Evaluate for malaria.
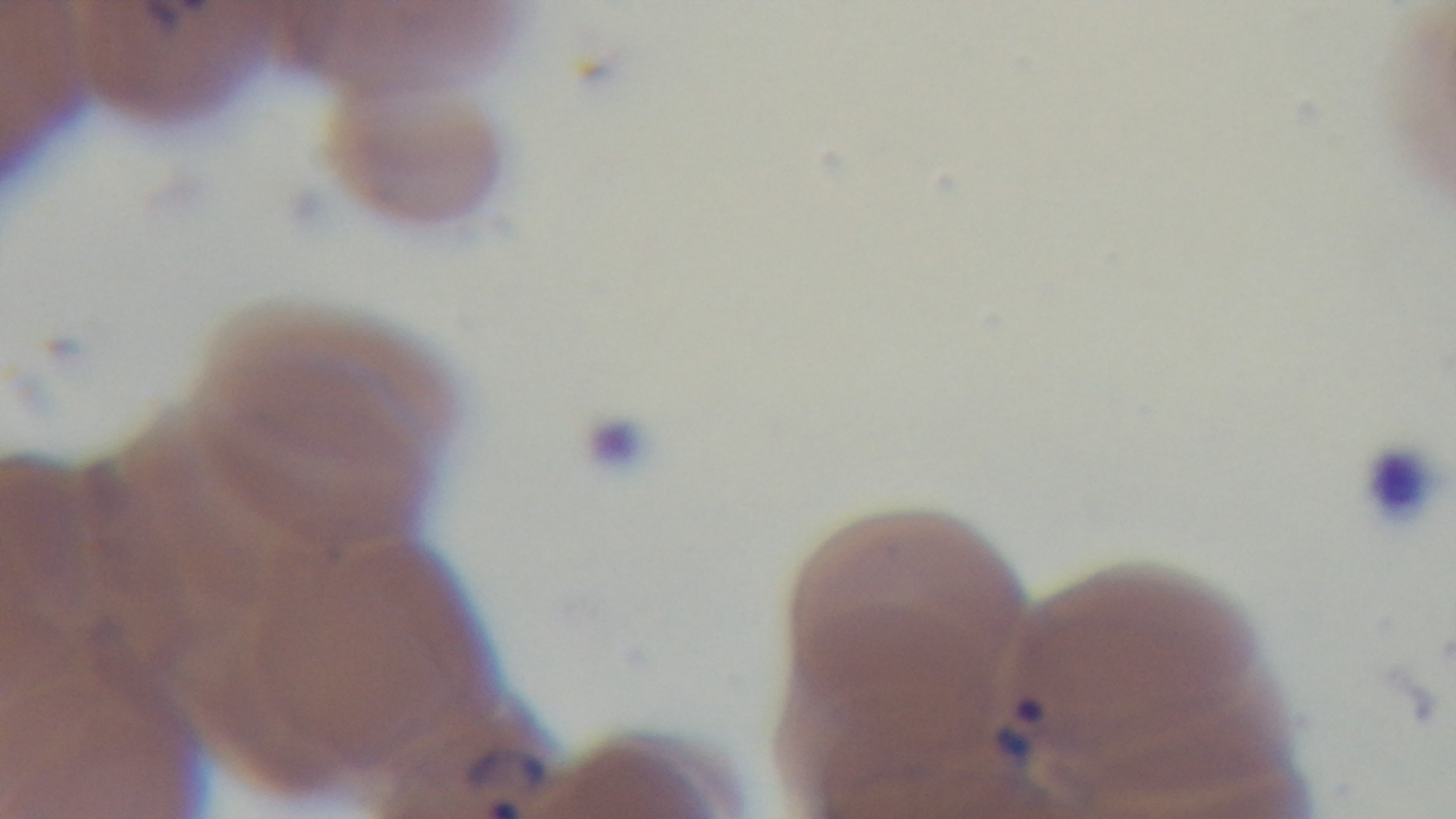
It is infected.

stain = Giemsa
field of view = single
modality = light microscopy
objective = 100x oil immersion
capture = mounted 4K digital camera
preparation = thin blood film